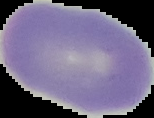
{
  "preparation": "thin blood smear",
  "malaria_status": "uninfected",
  "image_size": "154×118 pixels",
  "image_type": "segmented cell region with the area outside set to black"
}